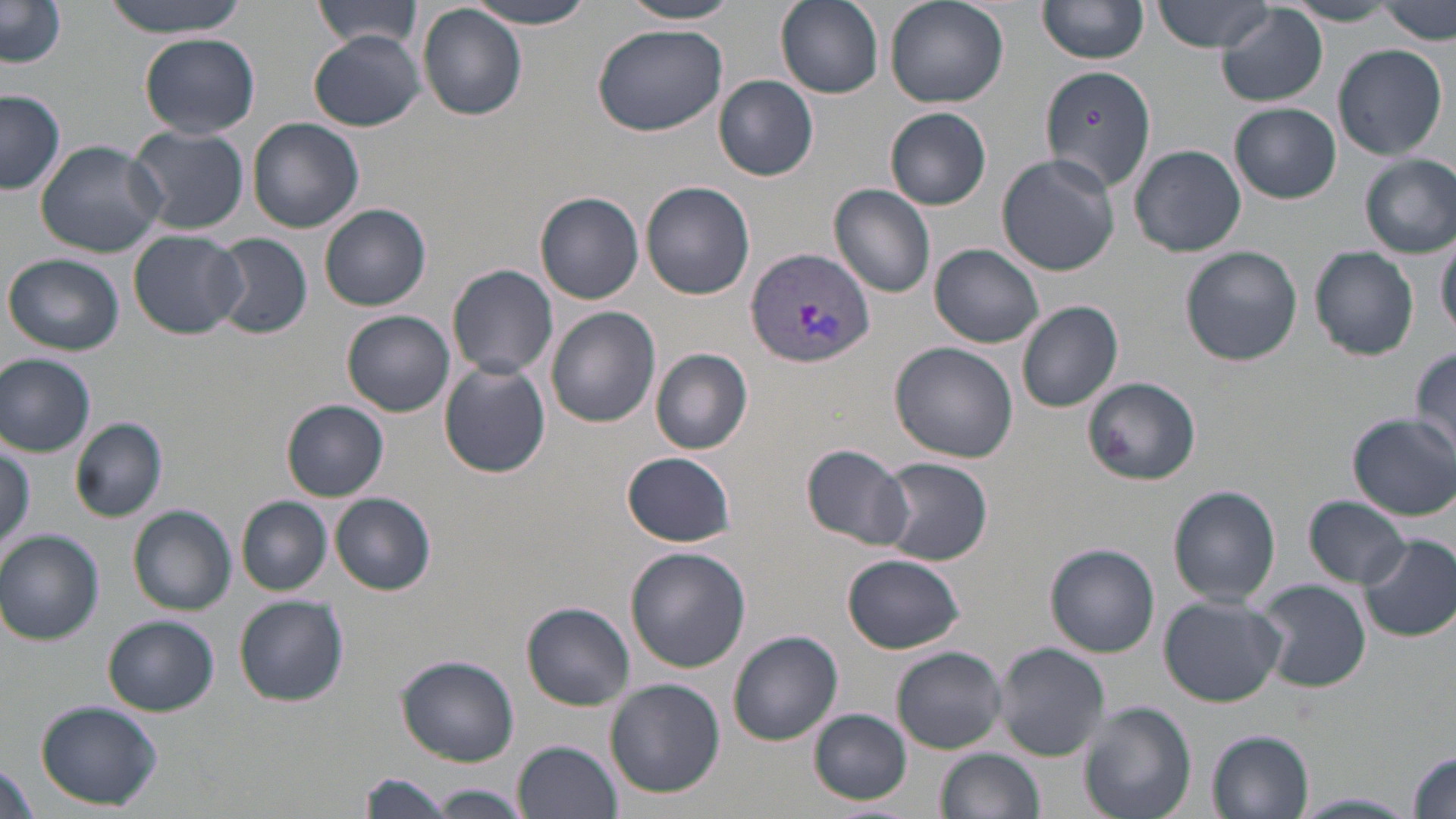 Approximate bounding boxes as [x1, y1, x2, y2] in pixels. Plasmodium vivax-infected red blood cell locations: [746, 248, 876, 366]. Uninfected red blood cell locations: [97, 0, 253, 35], [310, 0, 428, 50], [463, 0, 601, 30], [617, 0, 747, 25], [776, 0, 883, 97], [883, 0, 1009, 109], [1038, 1, 1148, 65], [1154, 1, 1279, 52], [0, 3, 67, 71], [1287, 3, 1401, 27], [1378, 3, 1456, 44], [417, 4, 528, 121], [1216, 5, 1328, 107], [592, 24, 728, 135], [141, 33, 259, 137], [308, 34, 426, 131], [1333, 44, 1447, 161], [1040, 65, 1156, 192], [713, 76, 820, 182], [0, 90, 66, 194], [1228, 102, 1342, 203], [885, 107, 991, 210], [248, 118, 364, 233], [127, 125, 249, 235], [34, 139, 167, 258], [1131, 144, 1246, 257], [997, 154, 1122, 276], [1360, 155, 1456, 257], [640, 181, 755, 300], [828, 185, 937, 297], [536, 192, 643, 305], [319, 204, 432, 311], [1437, 229, 1456, 337], [128, 231, 249, 340], [212, 233, 313, 339], [930, 244, 1044, 348], [1180, 246, 1303, 366], [1310, 247, 1419, 361], [5, 253, 125, 356], [447, 263, 559, 380], [1017, 301, 1124, 412], [548, 307, 662, 429], [343, 310, 454, 418], [888, 341, 1018, 462], [651, 348, 754, 454], [1410, 348, 1456, 458], [0, 354, 96, 455], [439, 362, 551, 479], [1082, 376, 1201, 488], [282, 400, 388, 500], [1348, 413, 1455, 519], [71, 417, 168, 522], [0, 442, 35, 557], [801, 442, 915, 551], [623, 452, 735, 547], [878, 457, 992, 566], [1168, 484, 1282, 607], [330, 492, 437, 596], [1304, 495, 1412, 589], [237, 496, 331, 596], [128, 506, 237, 615], [0, 530, 105, 644], [1358, 534, 1456, 643], [1045, 542, 1162, 656], [626, 547, 751, 672], [843, 553, 966, 653], [1254, 579, 1373, 693], [1160, 594, 1287, 706], [234, 596, 348, 707], [522, 602, 635, 709], [103, 615, 218, 715], [728, 630, 843, 744], [994, 644, 1110, 759], [891, 647, 1007, 753], [396, 653, 520, 766], [606, 679, 724, 798], [36, 701, 164, 810], [1079, 701, 1197, 819], [809, 710, 911, 804], [1208, 730, 1314, 817], [513, 738, 623, 819], [934, 747, 1044, 819], [1407, 750, 1455, 818], [0, 761, 41, 819], [356, 772, 457, 819], [427, 783, 531, 817], [1293, 792, 1421, 818]. Slide-level diagnosis: Plasmodium vivax. May-Grünwald-Giemsa-stained preparation. Light microscopy. Thin blood film. Captured at 1000x magnification. Single field of view. Image is 1456×819 pixels.